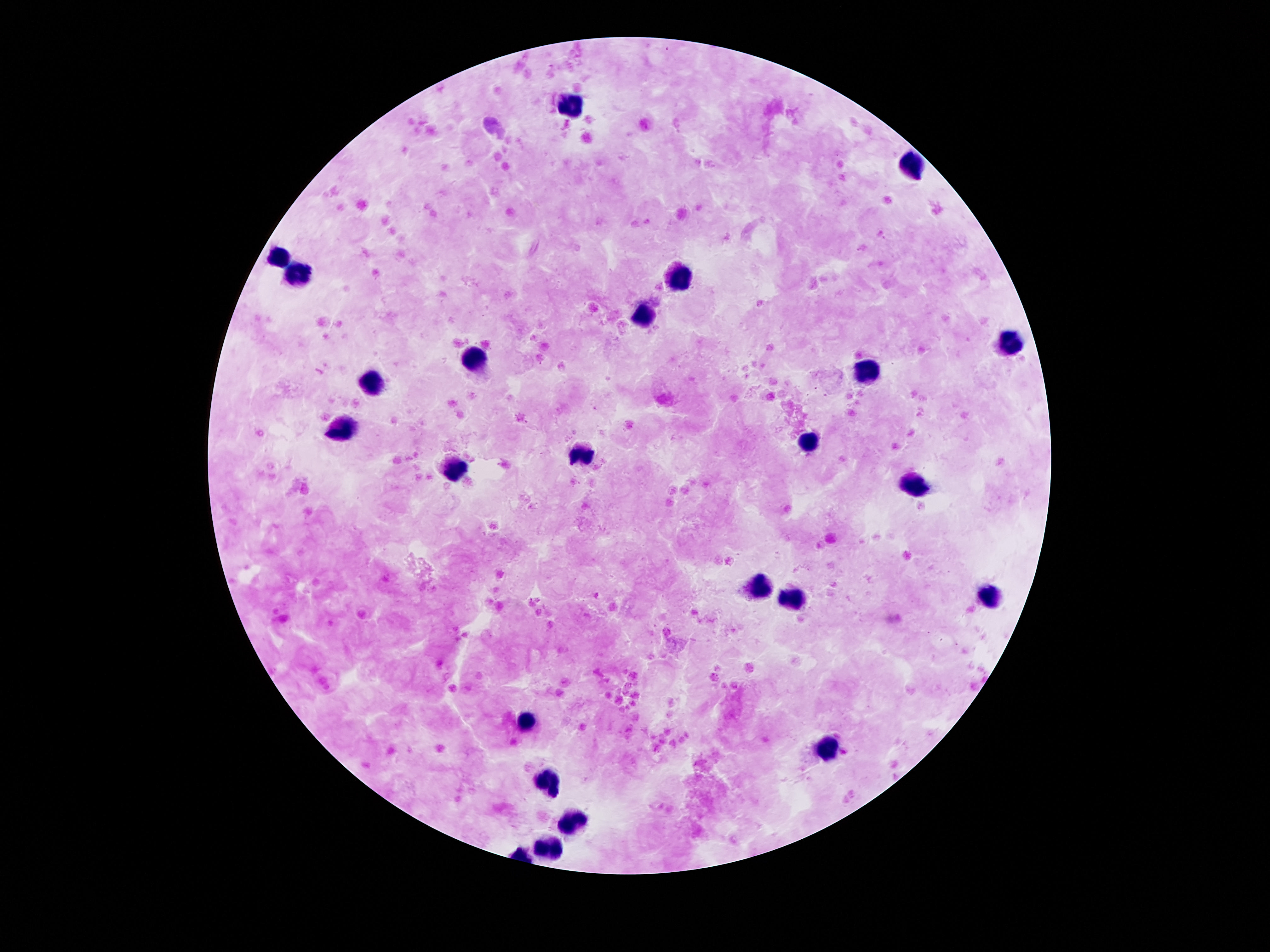

Approximate centers as {x, y} in pixels.
Summary:
  - Leukocyte locations: {572, 107}, {912, 166}, {279, 258}, {303, 277}, {680, 277}, {645, 312}, {1010, 344}, {477, 355}, {871, 369}, {373, 383}, {344, 430}, {807, 441}, {582, 453}, {451, 472}, {910, 484}, {754, 582}, {990, 595}, {797, 597}, {525, 720}, {828, 746}, {545, 779}, {574, 826}, {549, 853}
  - Image size: 1270×952 pixels
  - Capture: smartphone camera through the microscope eyepiece
  - Stain: Giemsa
  - Magnification: 100x
  - Field of view: single
  - Preparation: thick blood smear
  - Patient malaria status: not infected